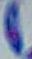

Summary:
  - Magnification: 1000x
  - Modality: photomicrograph
  - Identification: Toxoplasma gondii